Report the malaria status of this cell.
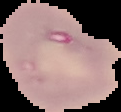

Parasitized.

{
  "preparation": "thin blood smear",
  "image_size": "121×112 pixels",
  "image_type": "segmented cell region on a black background"
}